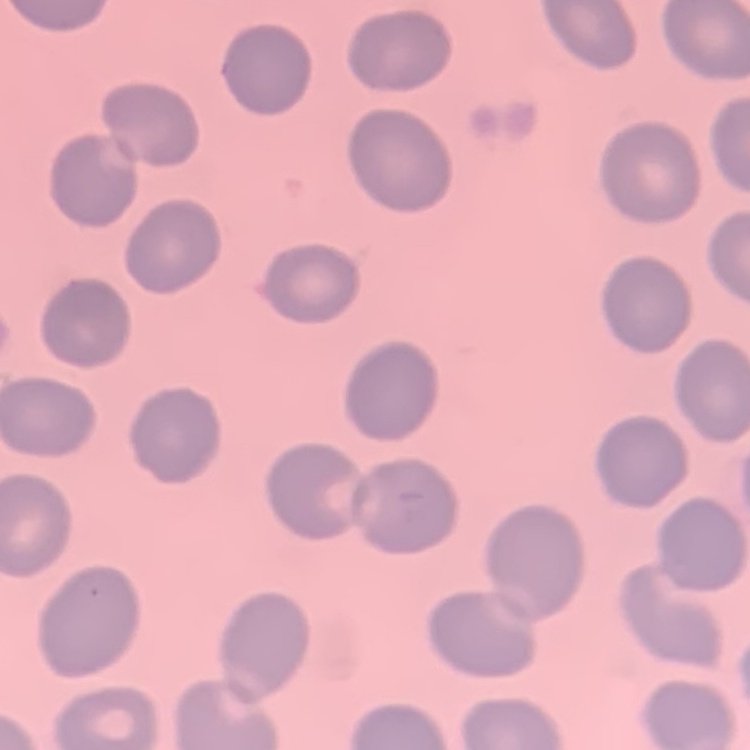
The erythrocytes exhibit no rouleaux formation. Thin blood smear. One tile cut from a larger photomicrograph. Stained with either Field's or Giemsa.